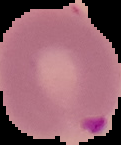

{
  "malaria_status": "parasitized",
  "image_size": "121×145 pixels",
  "preparation": "thin blood smear",
  "image_type": "cell region segmented out of the field of view; surrounding area masked to black"
}